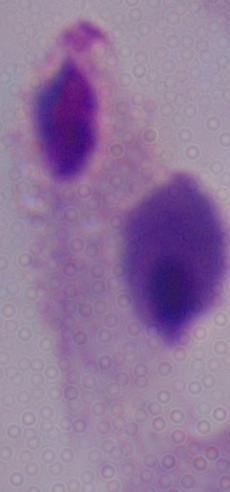

A trichomonad is seen. Photomicrograph. Captured at 1000x magnification.